Assess this cell for malaria.
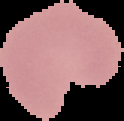

Parasitized.

image size = 124×121 pixels
preparation = thin blood smear
image type = segmented cell region on a black background